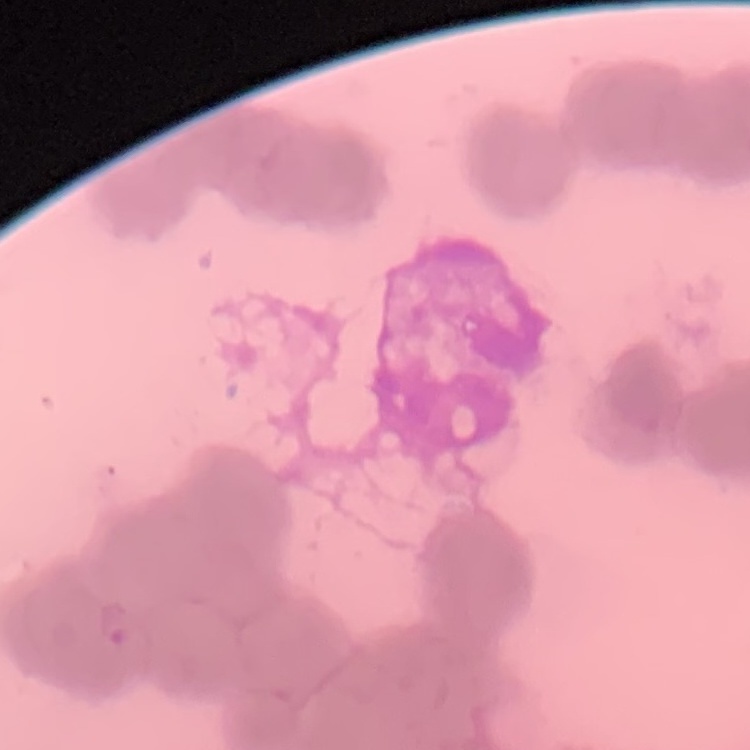

The erythrocytes show rouleaux formation. Stained with either Field's or Giemsa. Thin peripheral smear. Square crop of a larger photomicrograph.